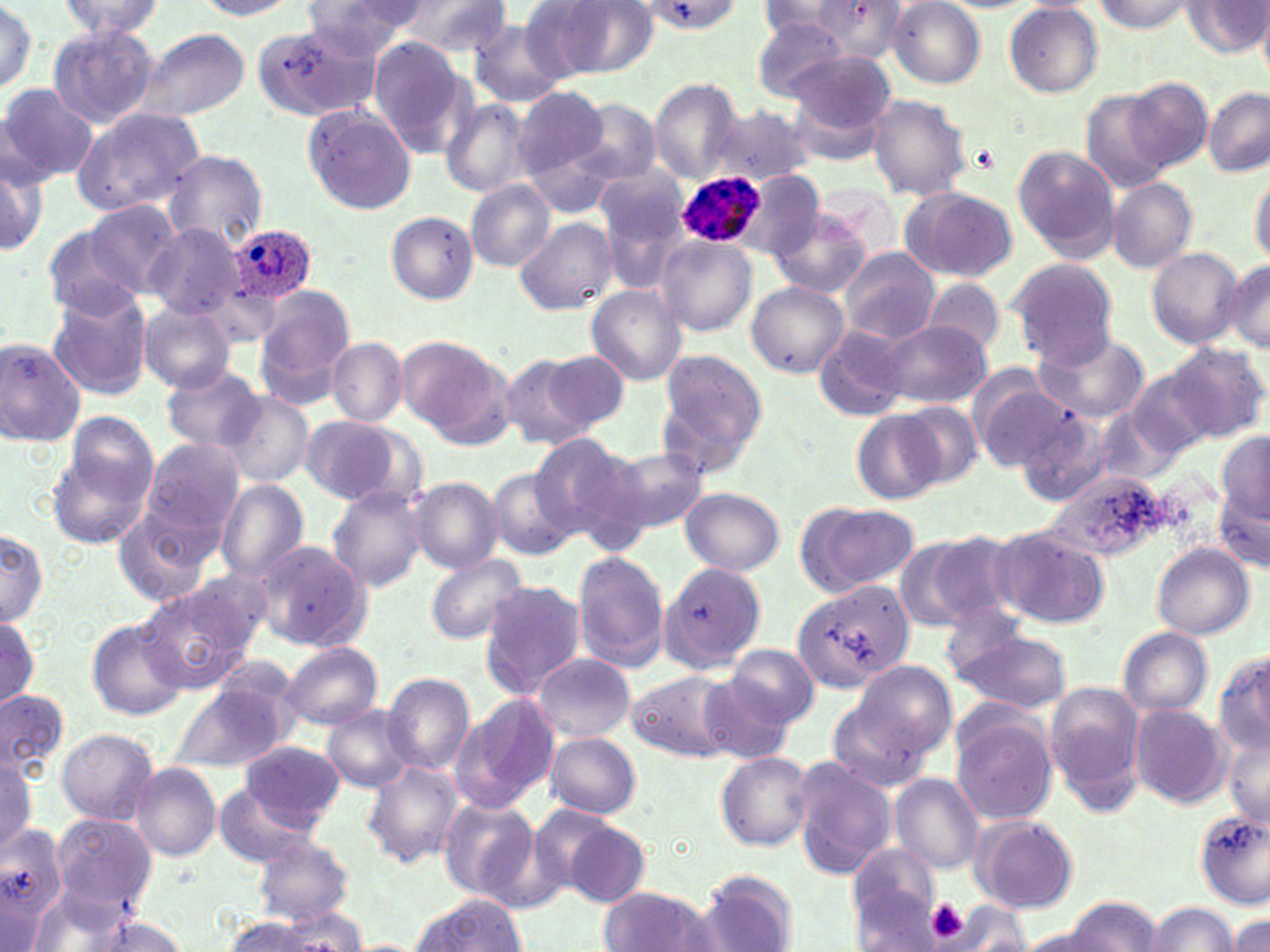

Approximate bounding boxes as named x1/y1/x2/y2 corners in pixels. Plasmodium ovale-infected red blood cell locations: (x1=675, y1=170, x2=765, y2=250), (x1=227, y1=222, x2=319, y2=308). Platelet locations: (x1=917, y1=898, x2=975, y2=943). Uninfected red blood cell locations: (x1=195, y1=0, x2=303, y2=19), (x1=305, y1=0, x2=424, y2=59), (x1=394, y1=0, x2=513, y2=54), (x1=789, y1=0, x2=905, y2=66), (x1=0, y1=1, x2=40, y2=97), (x1=59, y1=1, x2=164, y2=40), (x1=526, y1=1, x2=654, y2=80), (x1=1092, y1=1, x2=1204, y2=34), (x1=636, y1=2, x2=745, y2=34), (x1=756, y1=2, x2=865, y2=49), (x1=890, y1=2, x2=985, y2=86), (x1=1183, y1=2, x2=1267, y2=58), (x1=1006, y1=3, x2=1103, y2=99), (x1=1257, y1=12, x2=1270, y2=84), (x1=750, y1=16, x2=855, y2=101), (x1=250, y1=20, x2=375, y2=125), (x1=469, y1=20, x2=570, y2=107), (x1=47, y1=23, x2=160, y2=129), (x1=136, y1=28, x2=250, y2=121), (x1=367, y1=39, x2=469, y2=154), (x1=785, y1=55, x2=896, y2=165), (x1=1121, y1=76, x2=1213, y2=173), (x1=649, y1=77, x2=744, y2=184), (x1=0, y1=84, x2=96, y2=185), (x1=512, y1=85, x2=611, y2=184), (x1=1203, y1=86, x2=1269, y2=178), (x1=1079, y1=89, x2=1176, y2=193), (x1=867, y1=94, x2=972, y2=200), (x1=564, y1=97, x2=663, y2=186), (x1=439, y1=98, x2=535, y2=199), (x1=300, y1=102, x2=417, y2=214), (x1=713, y1=104, x2=814, y2=186), (x1=69, y1=107, x2=204, y2=218), (x1=517, y1=125, x2=621, y2=218), (x1=1013, y1=146, x2=1119, y2=260), (x1=0, y1=147, x2=47, y2=257), (x1=164, y1=150, x2=269, y2=252), (x1=595, y1=165, x2=692, y2=249), (x1=1250, y1=166, x2=1270, y2=266), (x1=740, y1=170, x2=825, y2=260), (x1=1107, y1=177, x2=1197, y2=272), (x1=465, y1=180, x2=555, y2=270), (x1=900, y1=186, x2=1017, y2=282), (x1=83, y1=198, x2=183, y2=297), (x1=770, y1=210, x2=870, y2=298), (x1=386, y1=212, x2=478, y2=305), (x1=513, y1=216, x2=615, y2=313), (x1=39, y1=222, x2=149, y2=318), (x1=146, y1=225, x2=248, y2=321), (x1=656, y1=234, x2=757, y2=336), (x1=1146, y1=246, x2=1244, y2=347), (x1=840, y1=248, x2=940, y2=344), (x1=1006, y1=257, x2=1117, y2=363), (x1=1225, y1=259, x2=1270, y2=354), (x1=920, y1=278, x2=1006, y2=356), (x1=746, y1=281, x2=849, y2=377), (x1=254, y1=284, x2=356, y2=402), (x1=45, y1=286, x2=154, y2=400), (x1=586, y1=287, x2=687, y2=386), (x1=139, y1=303, x2=235, y2=392), (x1=878, y1=320, x2=991, y2=408), (x1=813, y1=324, x2=911, y2=422), (x1=1028, y1=327, x2=1150, y2=422), (x1=0, y1=337, x2=86, y2=448), (x1=327, y1=337, x2=406, y2=425), (x1=395, y1=337, x2=505, y2=437), (x1=1167, y1=341, x2=1269, y2=443), (x1=542, y1=350, x2=628, y2=431), (x1=654, y1=350, x2=767, y2=476), (x1=501, y1=354, x2=597, y2=452), (x1=163, y1=367, x2=266, y2=453), (x1=968, y1=368, x2=1070, y2=470), (x1=1127, y1=369, x2=1213, y2=460), (x1=215, y1=390, x2=316, y2=488), (x1=900, y1=403, x2=983, y2=486), (x1=1011, y1=405, x2=1113, y2=509), (x1=853, y1=410, x2=948, y2=503), (x1=300, y1=415, x2=402, y2=505), (x1=45, y1=422, x2=162, y2=549), (x1=1217, y1=431, x2=1269, y2=522), (x1=531, y1=432, x2=648, y2=555), (x1=139, y1=438, x2=246, y2=543), (x1=603, y1=442, x2=707, y2=535), (x1=486, y1=467, x2=579, y2=561), (x1=1051, y1=473, x2=1170, y2=562), (x1=410, y1=477, x2=504, y2=573), (x1=215, y1=481, x2=310, y2=583), (x1=328, y1=484, x2=426, y2=591), (x1=1216, y1=485, x2=1270, y2=574), (x1=680, y1=487, x2=784, y2=576), (x1=795, y1=501, x2=921, y2=597), (x1=114, y1=507, x2=220, y2=609), (x1=992, y1=526, x2=1111, y2=630), (x1=0, y1=527, x2=47, y2=628), (x1=908, y1=531, x2=1021, y2=631), (x1=253, y1=539, x2=369, y2=651), (x1=1151, y1=544, x2=1254, y2=640), (x1=572, y1=552, x2=670, y2=672), (x1=423, y1=554, x2=528, y2=645), (x1=660, y1=562, x2=771, y2=675), (x1=186, y1=568, x2=275, y2=653), (x1=479, y1=580, x2=586, y2=699), (x1=790, y1=580, x2=911, y2=694), (x1=136, y1=583, x2=257, y2=693), (x1=0, y1=614, x2=42, y2=711), (x1=85, y1=618, x2=188, y2=721), (x1=951, y1=625, x2=1072, y2=713), (x1=1119, y1=627, x2=1214, y2=719), (x1=281, y1=642, x2=383, y2=730), (x1=727, y1=642, x2=819, y2=730), (x1=1215, y1=650, x2=1270, y2=756), (x1=530, y1=653, x2=636, y2=742), (x1=849, y1=660, x2=957, y2=760), (x1=627, y1=669, x2=740, y2=761), (x1=382, y1=672, x2=475, y2=774), (x1=699, y1=678, x2=792, y2=761), (x1=1045, y1=681, x2=1147, y2=813), (x1=169, y1=685, x2=287, y2=773), (x1=0, y1=686, x2=69, y2=777), (x1=448, y1=693, x2=560, y2=814), (x1=826, y1=696, x2=933, y2=795), (x1=1129, y1=703, x2=1229, y2=808), (x1=322, y1=705, x2=417, y2=792), (x1=950, y1=710, x2=1059, y2=826), (x1=56, y1=727, x2=158, y2=823), (x1=1222, y1=732, x2=1270, y2=828), (x1=545, y1=733, x2=641, y2=817), (x1=241, y1=740, x2=344, y2=828), (x1=715, y1=751, x2=813, y2=851), (x1=0, y1=755, x2=37, y2=853), (x1=790, y1=756, x2=897, y2=880), (x1=363, y1=761, x2=465, y2=867), (x1=131, y1=762, x2=222, y2=861), (x1=889, y1=774, x2=984, y2=875), (x1=212, y1=784, x2=318, y2=867), (x1=438, y1=796, x2=540, y2=901), (x1=522, y1=802, x2=621, y2=900), (x1=1194, y1=809, x2=1269, y2=907), (x1=51, y1=815, x2=158, y2=916), (x1=971, y1=816, x2=1079, y2=914), (x1=560, y1=820, x2=651, y2=909), (x1=0, y1=824, x2=69, y2=940), (x1=253, y1=837, x2=355, y2=923), (x1=848, y1=843, x2=943, y2=938), (x1=696, y1=871, x2=799, y2=952), (x1=598, y1=887, x2=713, y2=952), (x1=25, y1=892, x2=135, y2=952), (x1=405, y1=894, x2=530, y2=950), (x1=1065, y1=896, x2=1161, y2=951), (x1=944, y1=902, x2=1031, y2=949), (x1=1143, y1=902, x2=1239, y2=952), (x1=275, y1=906, x2=369, y2=949), (x1=1229, y1=911, x2=1269, y2=952), (x1=82, y1=915, x2=191, y2=952), (x1=219, y1=915, x2=324, y2=951), (x1=1013, y1=926, x2=1115, y2=952). Slide-level diagnosis: Plasmodium ovale. Image is 1270×952 pixels. 1000x magnification. Single field of view. May-Grünwald-Giemsa stain. Light microscopy. Thin blood smear.